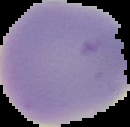

Image is 130×127 pixels. From a thin blood film. The area outside the segmented cell region is set to black. Malaria status: uninfected.